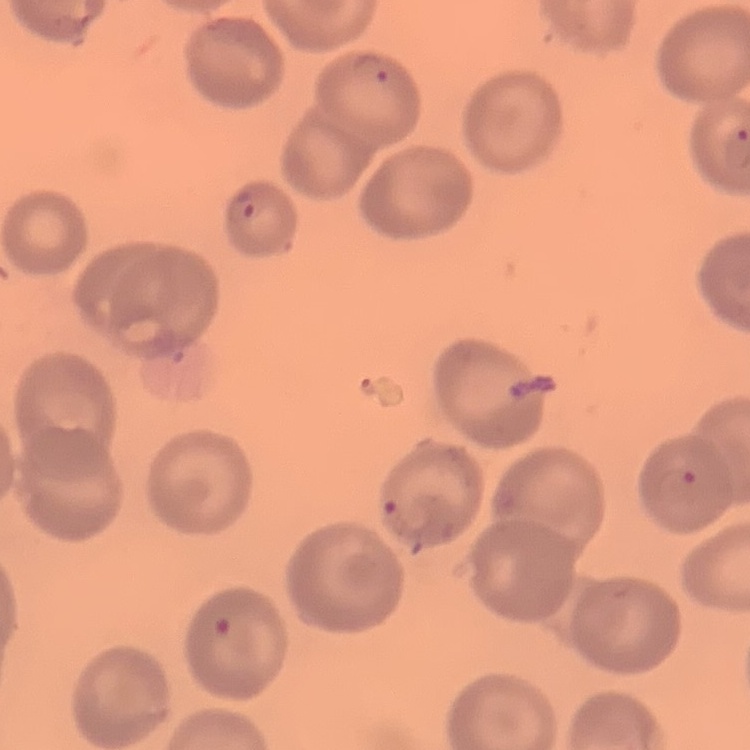

erythrocyte_morphology: no rouleaux formation
preparation: thin blood film
image_type: one tile cut from a larger photomicrograph
stain: Field's or Giemsa